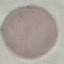

malaria status = uninfected
preparation = thin smear
image type = automatically extracted cell patch, resized to 64 × 64 pixels
capture = smartphone through the microscope eyepiece
stain = Giemsa